Name the parasite shown.
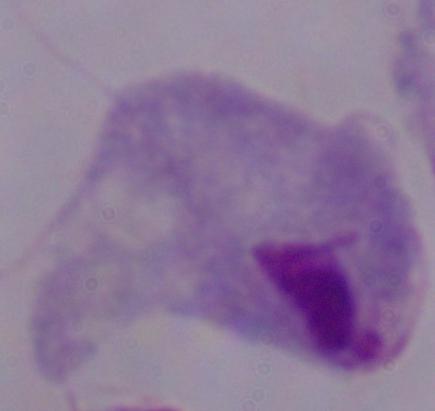
This is a trichomonad.

Summary:
  - Modality: photomicrograph
  - Magnification: 1000x